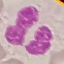
Malaria status: uninfected. Thin blood smear. Giemsa stain. Cell patch, automatically extracted from a larger field of view and resized to 64 × 64 pixels. Acquired by smartphone through the microscope eyepiece.